Assess for Plasmodium parasites.
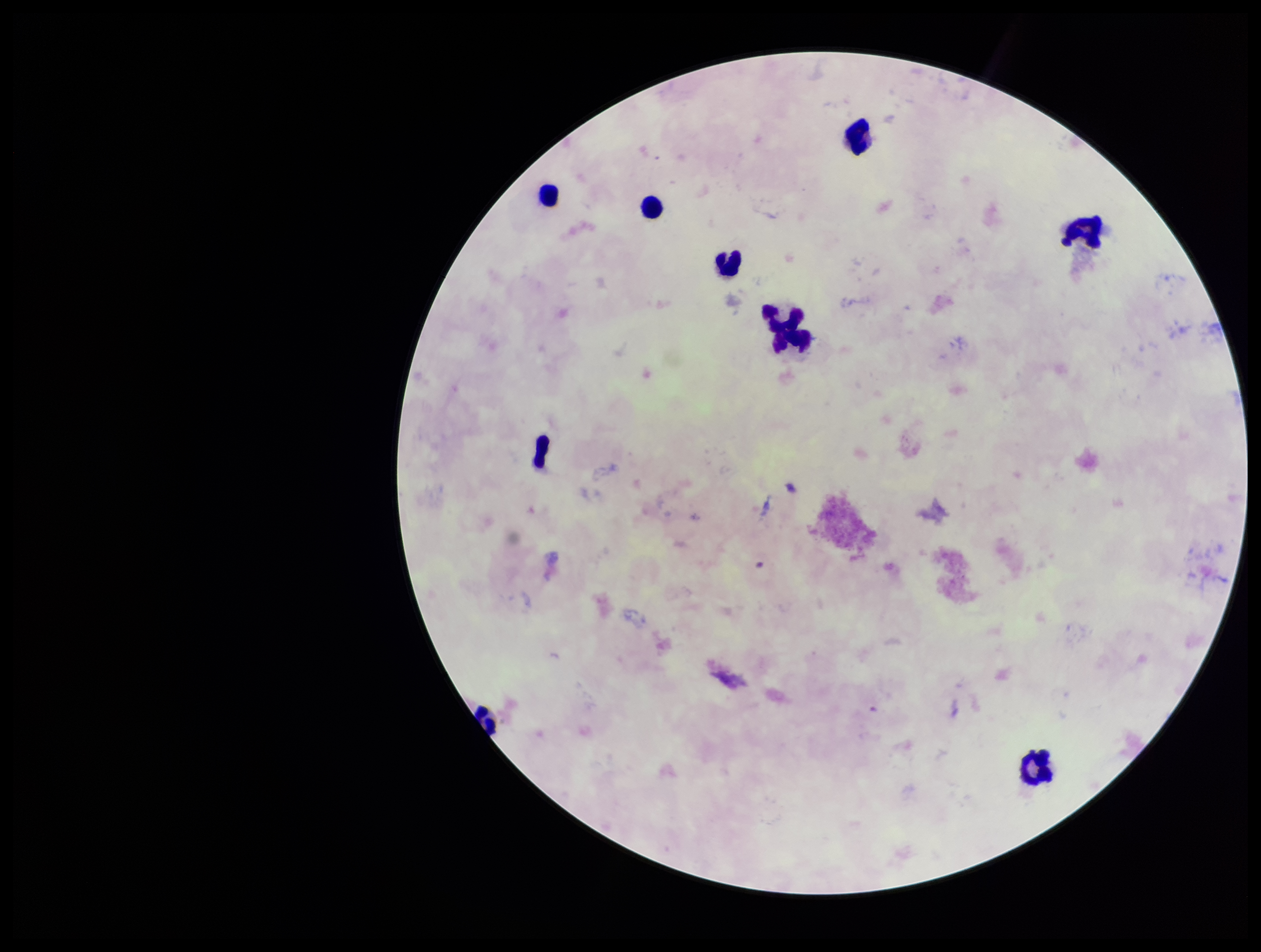
None identified.

Summary:
  - Preparation: thick smear
  - Image size: 1261×952 pixels
  - Leukocyte count: 10
  - Capture: smartphone photograph through the microscope eyepiece
  - Patient malaria status: infected
  - Parasite count: 0
  - Species reported for this patient: Plasmodium falciparum
  - Stain: Giemsa
  - Field of view: one from this slide